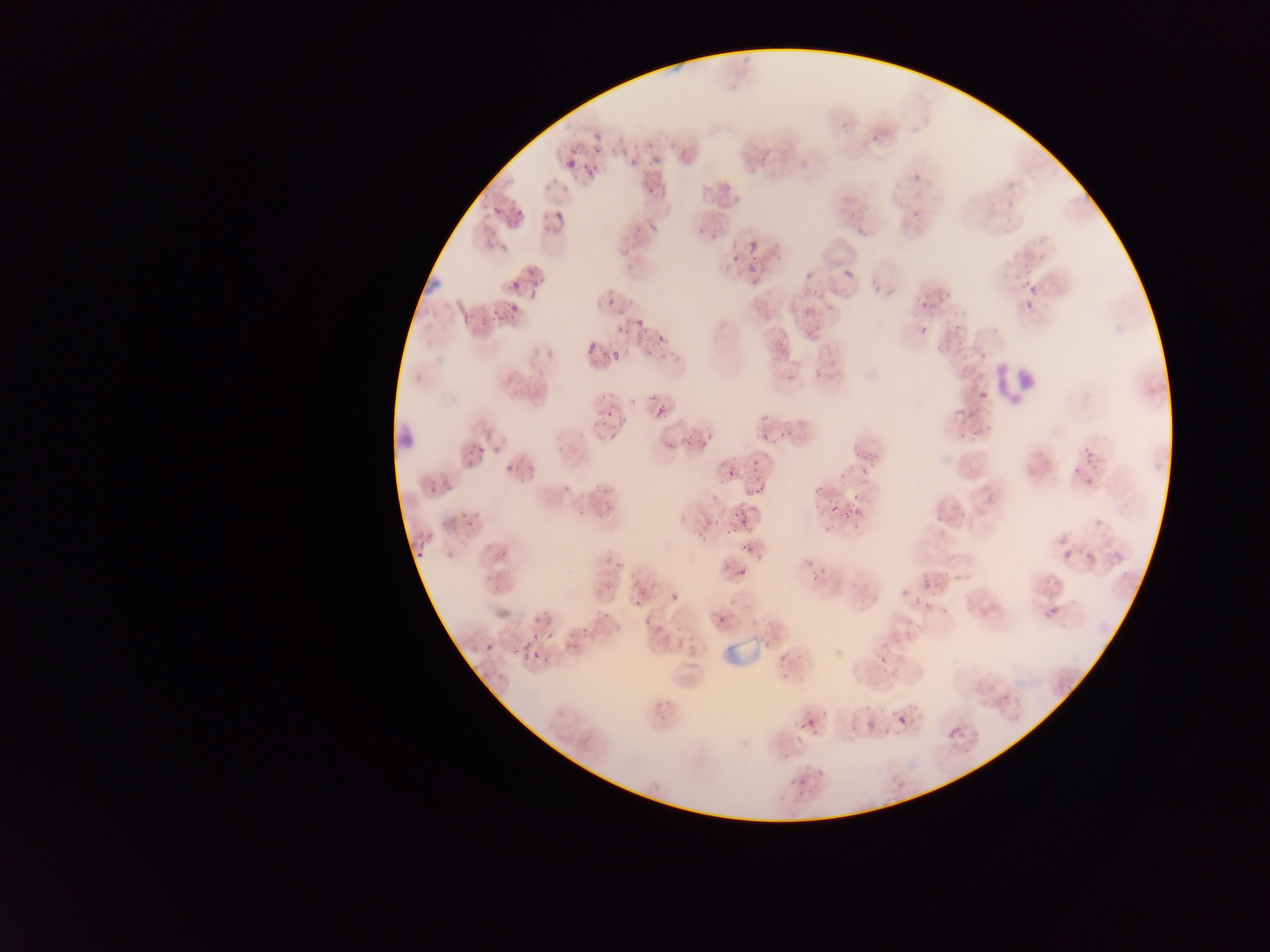

{
  "object_labeled_both_plasmodium_parasite_and_leukocyte_by_the_source": "approximate bounding boxes as (left, top, right, bottom) in pixels: (423, 272, 444, 293)",
  "field_of_view": "single",
  "country": "Ghana",
  "leukocyte_locations": "approximate bounding boxes as (left, top, right, bottom) in pixels: (993, 347, 1046, 409), (399, 426, 421, 450)",
  "plasmodium_parasite_locations": "approximate bounding boxes as (left, top, right, bottom) in pixels: (592, 141, 602, 153), (564, 156, 579, 170), (630, 156, 641, 168), (567, 159, 577, 169), (582, 166, 598, 180), (908, 168, 922, 182), (645, 186, 656, 196), (493, 206, 503, 215), (514, 208, 522, 219), (555, 212, 564, 222), (634, 221, 650, 234), (854, 224, 864, 239), (749, 241, 758, 251), (747, 255, 760, 274), (729, 256, 742, 262), (843, 268, 852, 276), (869, 268, 880, 283), (1024, 280, 1041, 296), (510, 281, 521, 292), (803, 284, 826, 295), (607, 299, 615, 308), (1022, 299, 1034, 311), (510, 303, 519, 312), (804, 303, 820, 314), (495, 311, 508, 322), (475, 312, 489, 328), (459, 313, 474, 325), (633, 319, 643, 330), (952, 323, 960, 331), (618, 326, 631, 335), (919, 326, 927, 335), (636, 332, 645, 346), (775, 332, 787, 345), (648, 336, 664, 350), (954, 336, 966, 350), (588, 345, 598, 355), (611, 351, 619, 361), (782, 370, 793, 382), (653, 392, 672, 416), (976, 392, 988, 403), (952, 404, 962, 416), (964, 407, 981, 419), (605, 408, 615, 418), (756, 415, 770, 424), (957, 425, 969, 438), (971, 429, 984, 437), (686, 431, 696, 443), (777, 431, 792, 442), (760, 432, 775, 443), (698, 433, 710, 451), (468, 439, 494, 459), (1078, 442, 1101, 469), (860, 450, 874, 465), (751, 453, 762, 464), (506, 456, 523, 475), (859, 467, 870, 473), (725, 468, 736, 478), (753, 470, 762, 479), (429, 476, 441, 489), (759, 481, 768, 491), (563, 485, 571, 493), (815, 487, 823, 494), (854, 492, 860, 500), (827, 500, 838, 514), (737, 501, 749, 512), (957, 502, 972, 516), (853, 508, 866, 515), (841, 509, 849, 520), (729, 512, 739, 517), (736, 518, 749, 526), (461, 520, 477, 531), (727, 527, 737, 534), (737, 540, 747, 552), (414, 549, 425, 561), (1062, 549, 1073, 560), (1084, 551, 1093, 563), (738, 568, 746, 578), (809, 569, 821, 583), (1045, 574, 1060, 588), (921, 578, 931, 590), (922, 589, 933, 612), (628, 591, 650, 611), (1048, 608, 1057, 621), (716, 613, 730, 631), (581, 618, 593, 639), (541, 620, 554, 642), (527, 632, 538, 641), (722, 636, 775, 673), (486, 643, 494, 653), (521, 644, 534, 657), (530, 644, 546, 664), (875, 650, 888, 663), (999, 692, 1015, 702), (659, 714, 667, 723), (898, 717, 906, 724), (799, 718, 815, 732), (865, 721, 873, 730), (942, 724, 963, 740), (818, 769, 826, 777), (797, 777, 807, 786) | approximate (x, y) pixel centers of objects too small to bound: (715, 519)",
  "image_size": "1270×952 pixels",
  "capture": "mobile-phone photograph through a microscope",
  "preparation": "thin blood smear"
}